Report the malaria status of this cell.
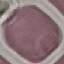
It is uninfected.

Thin blood film. Automatically extracted cell patch, resized to 64 × 64 pixels. Giemsa-stained preparation. Acquired by smartphone through the microscope eyepiece.